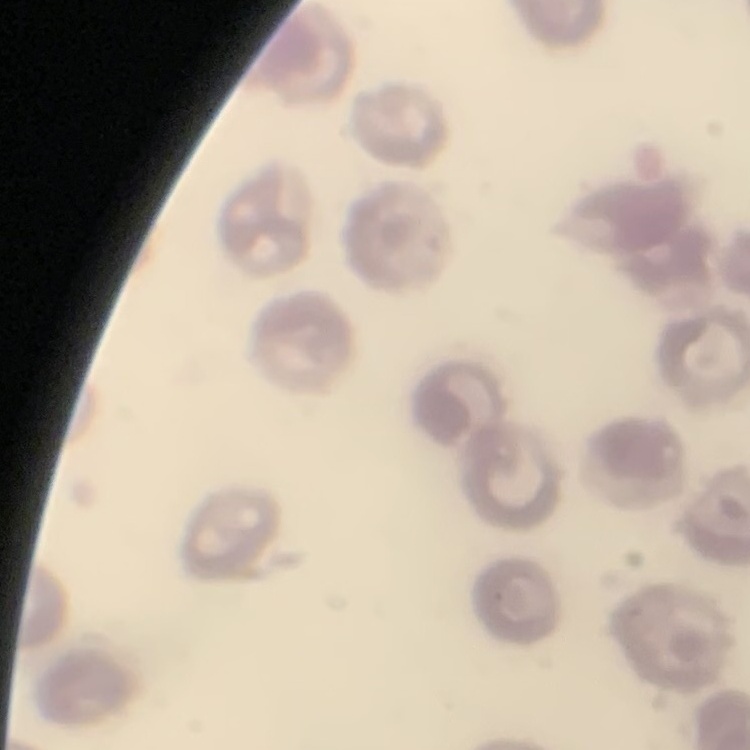
red blood cell morphology = no rouleaux formation
image type = square crop of a larger photomicrograph
preparation = thin blood smear
stain = Field's or Giemsa